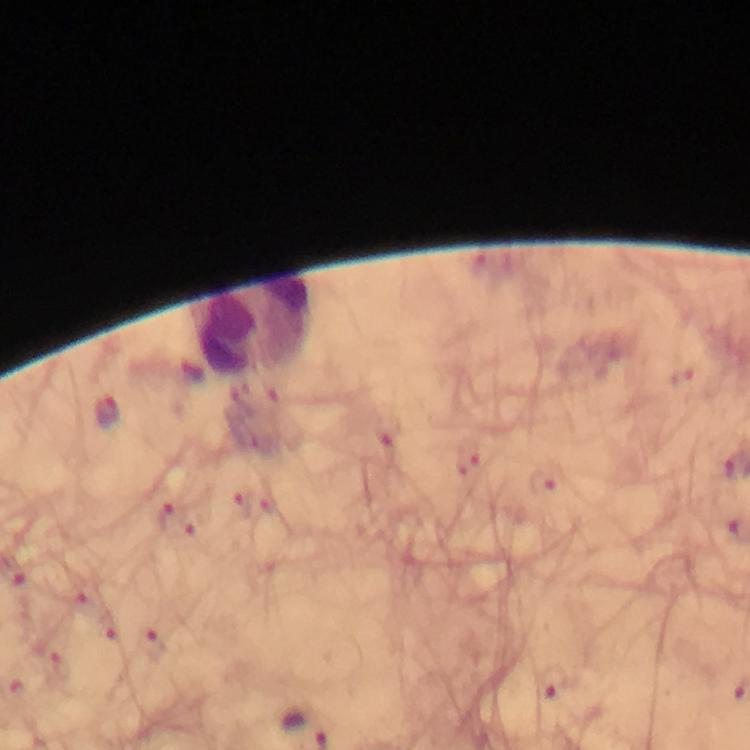

Approximate centers as (x, y) in pixels.
Summary:
  - Leukocyte locations: (251, 326)
  - Plasmodium parasite locations: (106, 413), (542, 482), (165, 516), (153, 643), (58, 665), (553, 682), (305, 725)
  - Cropped from: a single field of view
  - Immersion oil: applied
  - Capture: smartphone mounted on the microscope
  - Magnification: 100x
  - Context: from a diagnostic examination for malaria
  - Image size: 750×750 pixels
  - Preparation: thick blood film
  - Stain: Giemsa